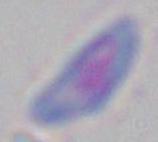 Captured at 1000x magnification. Toxoplasma gondii is seen. Micrograph.